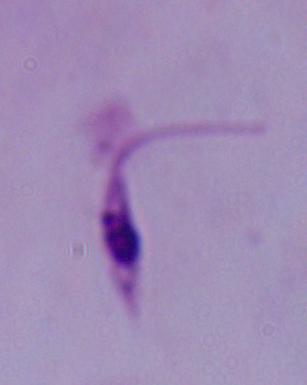

A Leishmania parasite is shown. Micrograph. Captured at 1000x magnification.